Assess this cell for malaria.
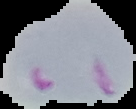
It is parasitized.

The area outside the segmented cell region is set to black. Image is 136×109 pixels. From a thin blood film.